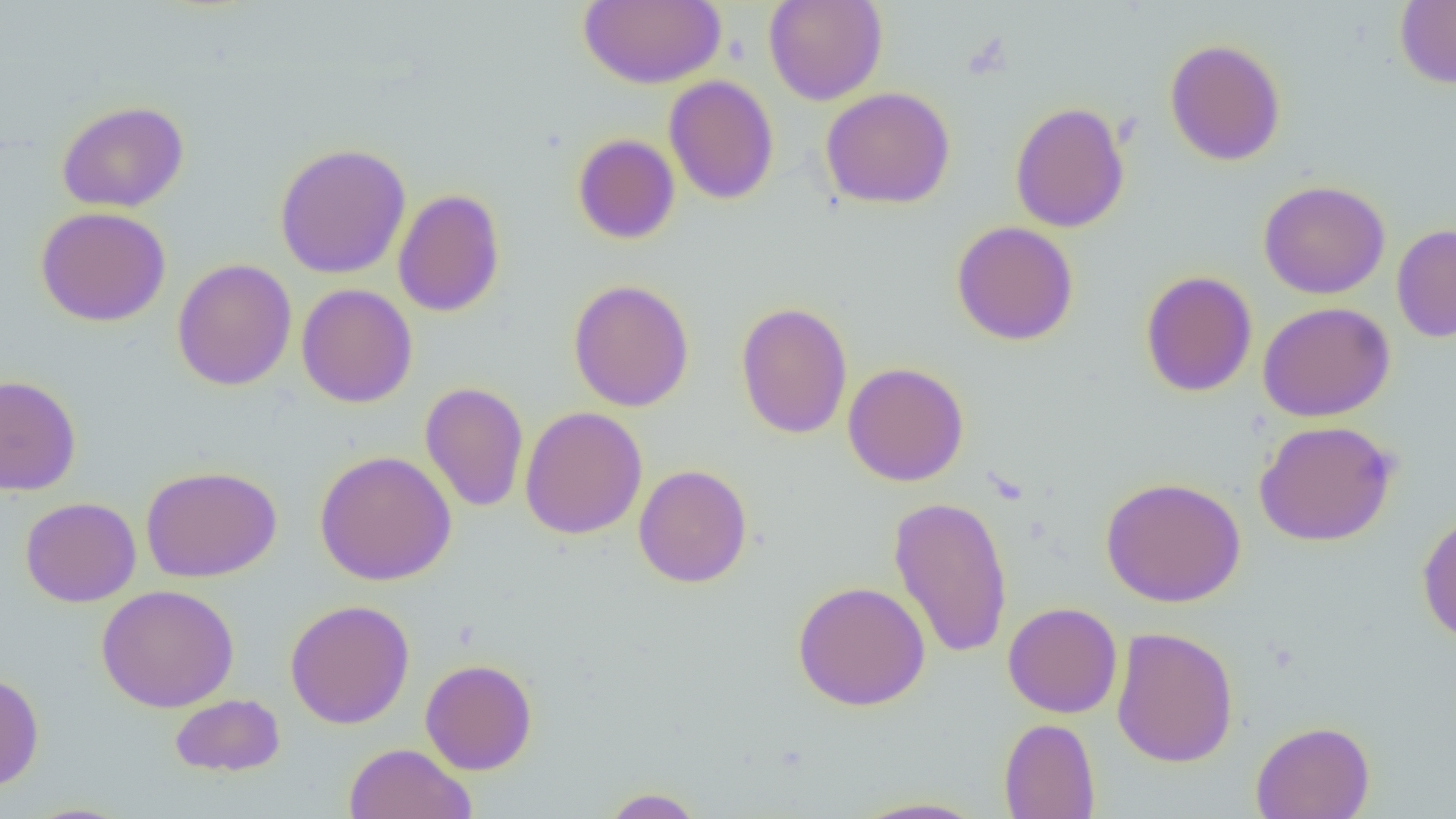 Approximate bounding boxes as (x1,y1)-(x2,y2) corner pairs in pixels. Uninfected red blood cell locations: (578,0)-(726,89), (762,0)-(888,106), (1395,0)-(1456,89), (1164,38)-(1286,166), (663,75)-(779,205), (820,86)-(956,210), (57,101)-(189,213), (1010,101)-(1130,233), (572,134)-(680,244), (274,142)-(412,279), (1258,179)-(1391,299), (392,188)-(505,318), (35,206)-(171,326), (951,221)-(1079,346), (1392,224)-(1456,343), (172,258)-(297,391), (1140,270)-(1258,397), (568,279)-(695,412), (296,284)-(418,408), (736,301)-(853,439), (1258,301)-(1396,422), (842,362)-(970,486), (0,373)-(81,496), (419,381)-(529,512), (416,393)-(646,518), (519,406)-(648,540), (1254,420)-(1398,546), (314,450)-(456,585), (634,464)-(752,588), (141,465)-(281,583), (1100,476)-(1246,607), (887,495)-(1013,660), (20,496)-(141,607), (1416,508)-(1456,645), (792,580)-(931,711), (96,584)-(239,713), (284,599)-(415,729), (1003,602)-(1122,719), (1110,625)-(1240,768), (420,659)-(537,775), (0,671)-(44,791), (169,693)-(285,777), (999,718)-(1101,819), (1250,720)-(1375,819), (343,743)-(476,819), (600,787)-(706,818), (847,796)-(990,818), (19,802)-(137,819). Slide-level diagnosis: negative for blood parasites. Captured at 1000x magnification. One field of a larger specimen. Optical microscopy. Thin blood smear. Image is 1456×819 pixels.